Assess this cell for malaria.
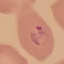
Parasitized.

preparation: thin blood film
image_type: cell patch, automatically extracted from a larger field of view and resized to 64 × 64 pixels
capture: smartphone camera at the microscope eyepiece
stain: Giemsa